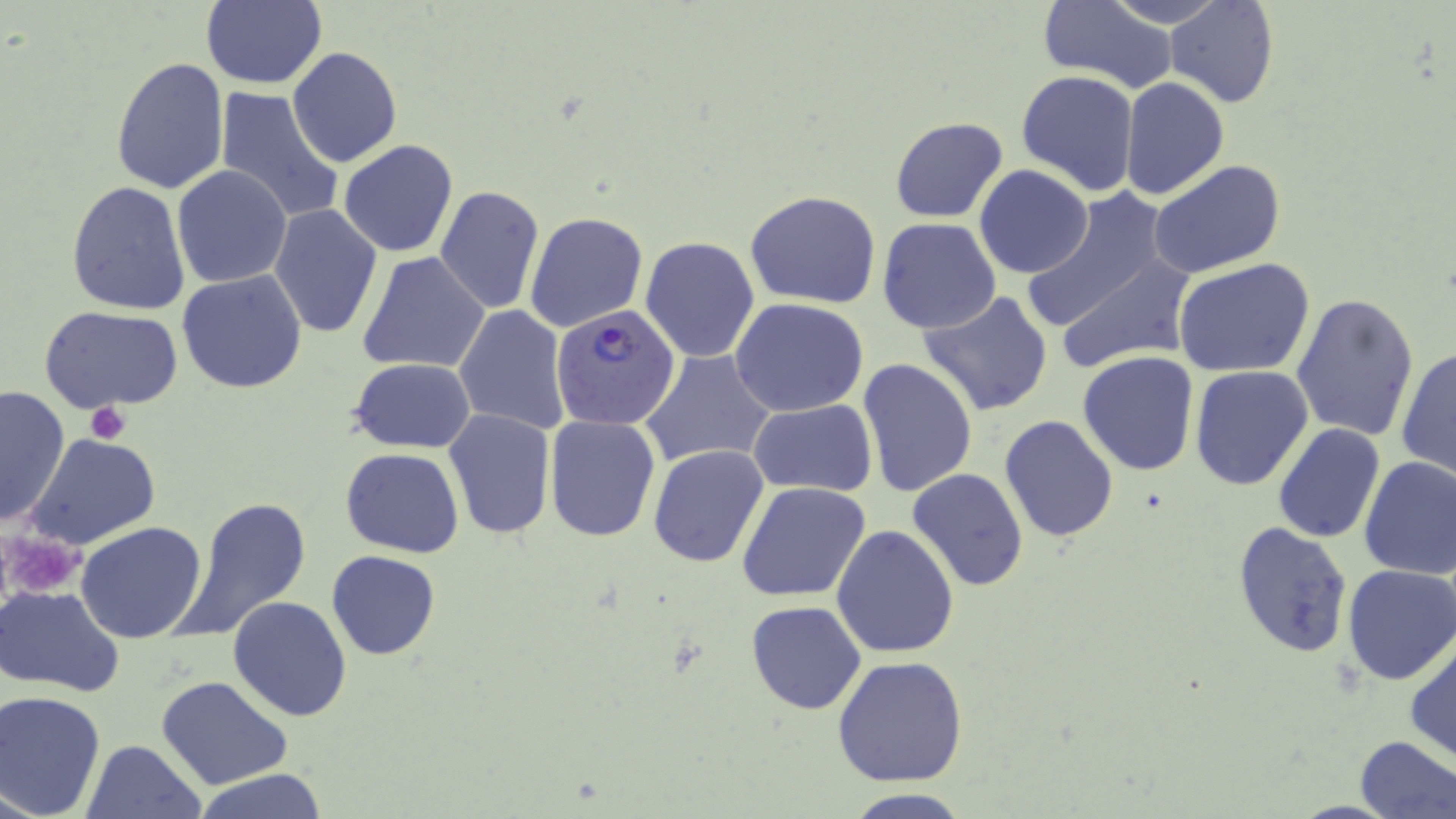
Plasmodium falciparum-infected red blood cell locations = approximate bounding boxes as [x1, y1, x2, y2] in pixels: [550, 303, 679, 430]
slide-level diagnosis = Plasmodium falciparum
field of view = one of a larger specimen
image size = 1456×819 pixels
preparation = thin blood film
uninfected red blood cell locations = approximate bounding boxes as [x1, y1, x2, y2] in pixels: [1100, 0, 1231, 29], [201, 1, 327, 89], [1036, 1, 1177, 91], [1165, 1, 1280, 107], [287, 47, 404, 168], [111, 56, 229, 193], [1016, 70, 1140, 196], [1120, 78, 1229, 201], [214, 87, 345, 225], [890, 116, 1009, 223], [338, 140, 458, 257], [1148, 159, 1287, 280], [171, 165, 292, 288], [975, 165, 1092, 278], [65, 181, 192, 316], [433, 185, 545, 317], [1019, 189, 1175, 338], [745, 190, 883, 310], [269, 203, 382, 339], [525, 210, 649, 334], [877, 218, 1002, 334], [641, 235, 761, 362], [1051, 251, 1195, 373], [358, 252, 489, 375], [1174, 257, 1316, 377], [178, 271, 307, 394], [917, 291, 1055, 417], [1291, 292, 1420, 442], [730, 298, 869, 417], [453, 304, 569, 435], [41, 306, 184, 412], [1396, 345, 1456, 482], [639, 348, 776, 470], [1077, 351, 1201, 477], [349, 358, 476, 452], [858, 358, 979, 498], [1189, 366, 1314, 491], [0, 383, 72, 526], [747, 398, 878, 496], [444, 409, 556, 539], [544, 414, 663, 542], [1000, 414, 1119, 543], [1272, 422, 1386, 542], [27, 432, 160, 549], [648, 445, 770, 568], [340, 447, 464, 559], [1358, 455, 1456, 580], [907, 468, 1031, 593], [737, 481, 872, 603], [174, 497, 313, 640], [76, 522, 207, 644], [1233, 522, 1354, 658], [831, 525, 960, 659], [326, 551, 441, 660], [1341, 565, 1456, 685], [0, 585, 127, 698], [227, 595, 353, 723], [745, 601, 867, 715], [1404, 634, 1456, 764], [830, 656, 970, 787], [157, 676, 293, 791], [0, 690, 107, 818], [1354, 734, 1456, 818], [80, 739, 204, 819], [193, 769, 328, 819], [838, 789, 979, 819]
magnification = 1000x
modality = optical microscopy
stain = May-Grünwald-Giemsa
platelet locations = approximate bounding boxes as [x1, y1, x2, y2] in pixels: [86, 402, 131, 446], [3, 527, 88, 602]